Classify this cell by malaria status.
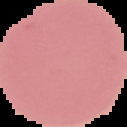
It is uninfected.

Summary:
  - Image type: cell region segmented out of the field of view; surrounding area masked to black
  - Preparation: thin blood smear
  - Image size: 127×127 pixels